Locate every leukocyte (white blood cell).
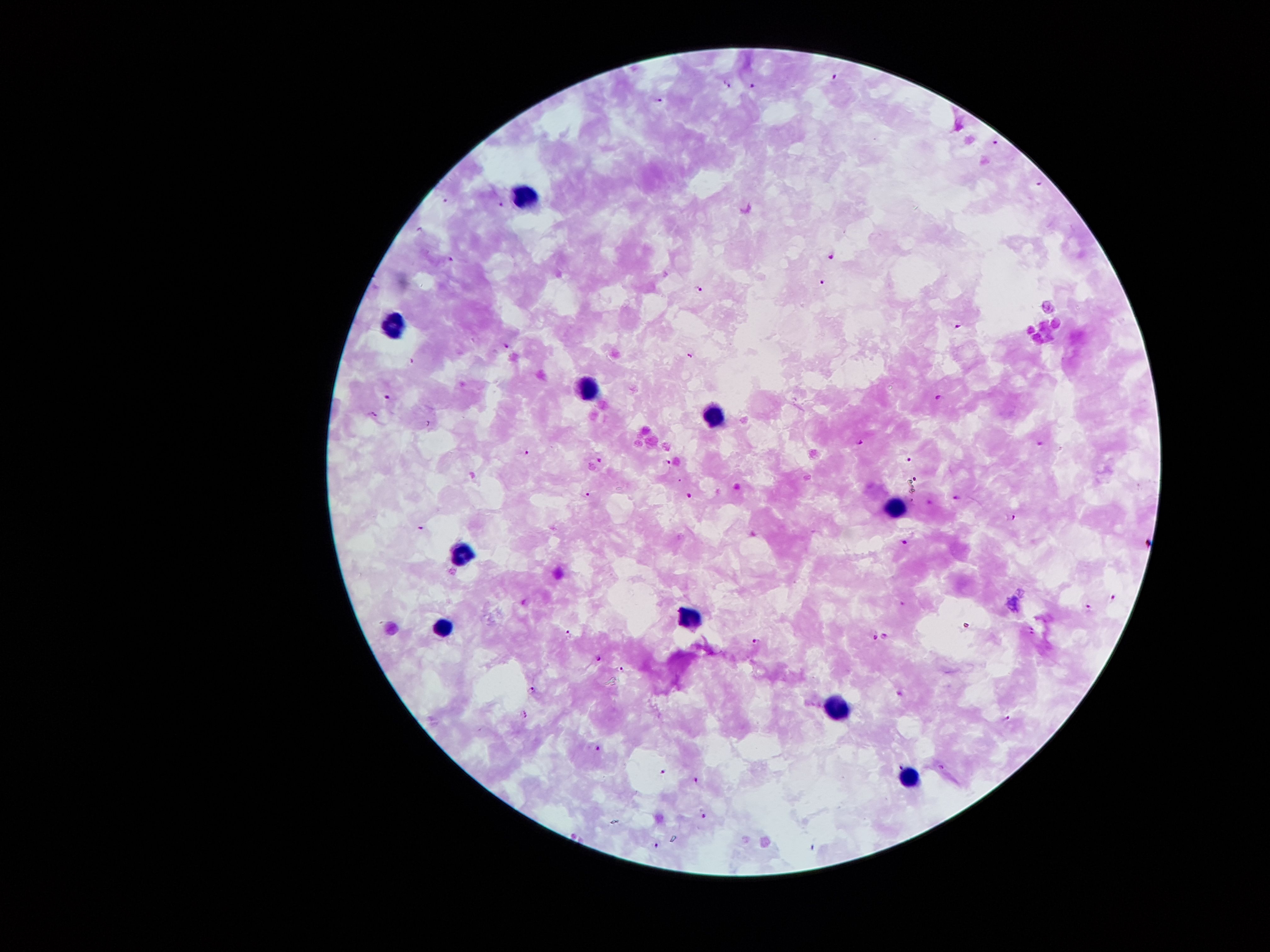

Approximate centers as (x, y) in pixels.
Leukocytes: (522, 190), (391, 321), (587, 389), (714, 416), (891, 506), (460, 553), (685, 619), (440, 626), (835, 703), (911, 781).

Plasmodium parasite locations = (835, 77), (728, 85), (752, 85), (658, 100), (994, 140), (1040, 179), (446, 199), (501, 204), (419, 230), (832, 254), (450, 261), (822, 281), (699, 289), (958, 327), (506, 346), (691, 353), (387, 396), (940, 396), (374, 413), (860, 443), (1040, 443), (527, 452), (598, 459), (910, 459), (668, 462), (679, 479), (916, 479), (588, 493), (689, 495), (957, 497), (911, 498), (929, 501), (1014, 517), (422, 528), (905, 541), (1113, 598), (525, 602), (903, 604), (1086, 608), (1032, 630), (568, 632), (885, 636), (875, 638), (754, 641), (599, 658), (620, 669), (532, 688), (525, 713), (1008, 718), (597, 747), (901, 766), (941, 767), (663, 770), (696, 781), (702, 814), (656, 844)
stain = Giemsa
capture = smartphone through the microscope eyepiece
patient malaria status = positive for Plasmodium falciparum
preparation = thick peripheral-blood smear
image size = 1270×952 pixels
magnification = 100x
field of view = one from this slide